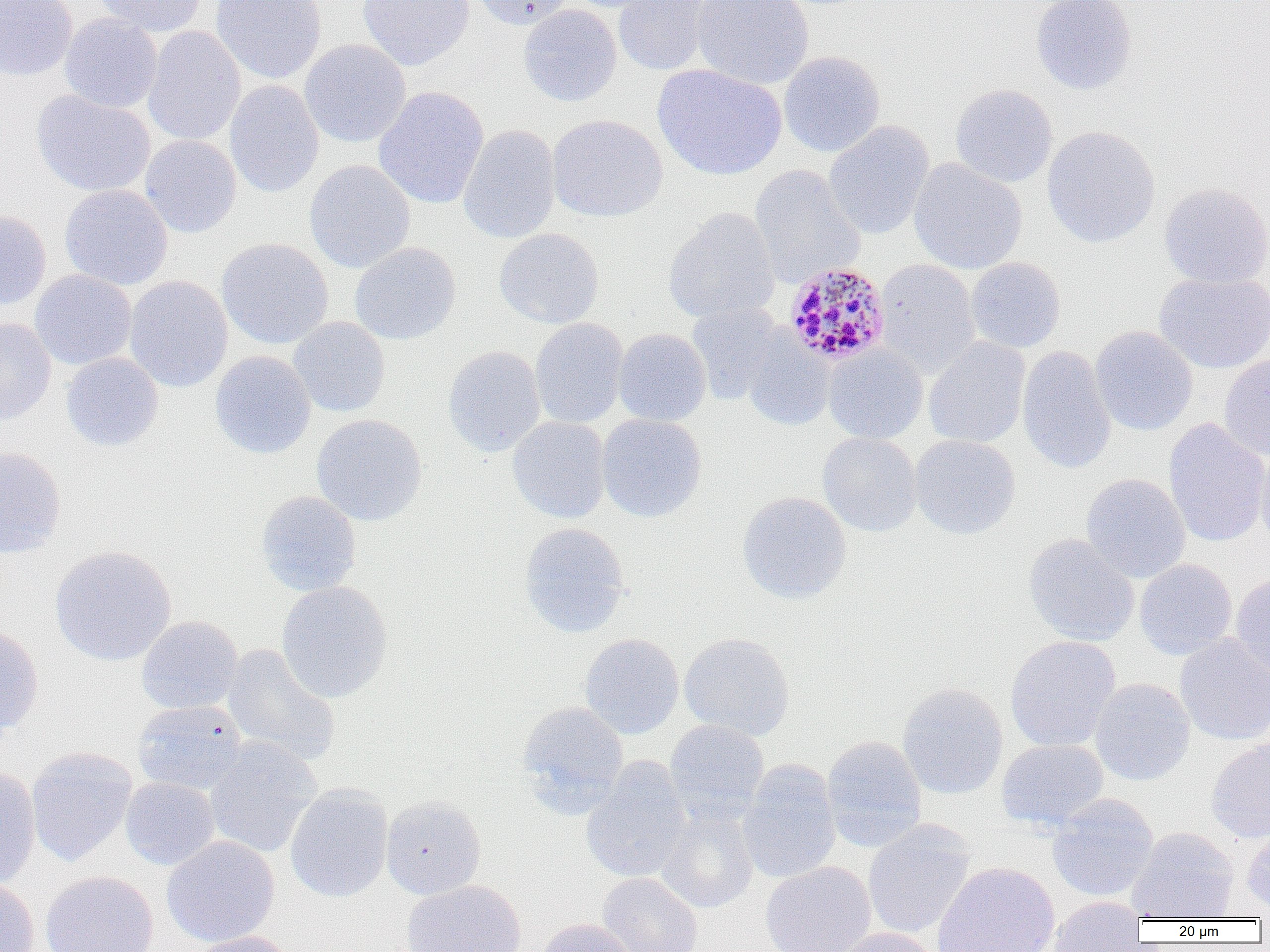
Summary:
  - Coordinate format: approximate bounding boxes as (x1,y1)-(x2,y2) corner pairs in pixels
  - Plasmodium malariae-infected red blood cell locations: (782,262)-(891,366)
  - Uninfected red blood cell locations: (0,0)-(78,81), (91,0)-(207,36), (210,0)-(327,84), (358,0)-(474,70), (471,0)-(574,29), (560,0)-(668,13), (614,0)-(713,76), (692,0)-(815,90), (1030,0)-(1137,95), (518,4)-(622,107), (59,14)-(162,112), (142,26)-(246,146), (299,39)-(411,147), (778,51)-(885,157), (653,64)-(787,180), (224,80)-(324,198), (950,84)-(1058,188), (373,86)-(489,208), (32,90)-(156,197), (547,114)-(667,222), (823,121)-(934,239), (458,125)-(561,244), (1041,125)-(1160,248), (140,134)-(241,237), (908,158)-(1028,274), (304,159)-(415,273), (749,164)-(865,288), (1159,183)-(1270,288), (59,184)-(173,290), (663,208)-(780,324), (0,211)-(52,309), (494,228)-(604,329), (216,238)-(334,349), (349,242)-(461,345), (965,257)-(1066,353), (875,259)-(980,378), (29,270)-(137,370), (1154,271)-(1270,374), (124,275)-(233,393), (687,302)-(785,405), (287,316)-(390,417), (0,317)-(57,424), (530,318)-(629,429), (1090,326)-(1198,436), (614,328)-(711,426), (742,332)-(835,431), (923,336)-(1030,448), (823,344)-(928,444), (1017,345)-(1116,475), (443,346)-(546,456), (210,351)-(316,459), (61,352)-(164,451), (1219,353)-(1270,460), (596,413)-(707,522), (311,414)-(427,526), (508,415)-(611,523), (1163,418)-(1270,547), (818,432)-(922,536), (909,435)-(1021,540), (1254,443)-(1270,550), (0,446)-(67,558), (1081,473)-(1190,582), (255,490)-(362,595), (736,491)-(852,604), (519,522)-(630,638), (1024,533)-(1139,646), (50,545)-(176,666), (1134,559)-(1237,660), (1230,572)-(1270,677), (276,580)-(393,703), (136,616)-(243,714), (0,626)-(44,735), (679,632)-(795,740), (579,633)-(684,740), (1174,634)-(1270,746), (1005,635)-(1120,752), (221,643)-(341,768), (1089,677)-(1195,785), (897,683)-(1008,799), (132,700)-(247,795), (517,701)-(628,812), (664,719)-(769,825), (821,735)-(927,851), (203,736)-(322,858), (996,738)-(1109,831), (1206,739)-(1270,843), (26,746)-(138,867), (580,756)-(692,883), (736,759)-(842,884), (0,765)-(41,891), (120,777)-(220,870), (284,783)-(393,902), (1047,794)-(1159,901), (380,795)-(486,899), (655,805)-(759,913), (862,822)-(975,939), (1242,826)-(1270,915), (1127,827)-(1239,921), (161,835)-(280,947), (760,861)-(877,952), (932,861)-(1060,952), (40,871)-(159,952), (596,872)-(704,952), (0,877)-(39,952), (402,880)-(526,952), (1043,896)-(1146,952), (533,918)-(638,952), (828,928)-(943,952), (185,931)-(297,952)
  - Slide-level diagnosis: Plasmodium malariae
  - Image size: 1270×952 pixels
  - Modality: light microscopy
  - Preparation: thin blood film
  - Magnification: 1000x
  - Field of view: single